Classify this cell by malaria status.
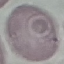
Uninfected.

image type = cell patch, automatically extracted from a larger field of view and resized to 64 × 64 pixels
capture = smartphone camera at the microscope eyepiece
stain = Giemsa
preparation = thin smear